Assess this cell for malaria.
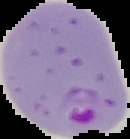

It is parasitized.

preparation = thin blood smear
image type = segmented cell region with the area outside set to black
image size = 130×139 pixels